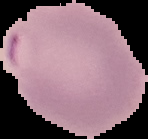

Summary:
  - Malaria status: parasitized
  - Preparation: thin blood smear
  - Image size: 148×139 pixels
  - Image type: cell region segmented out of the field of view; surrounding area masked to black